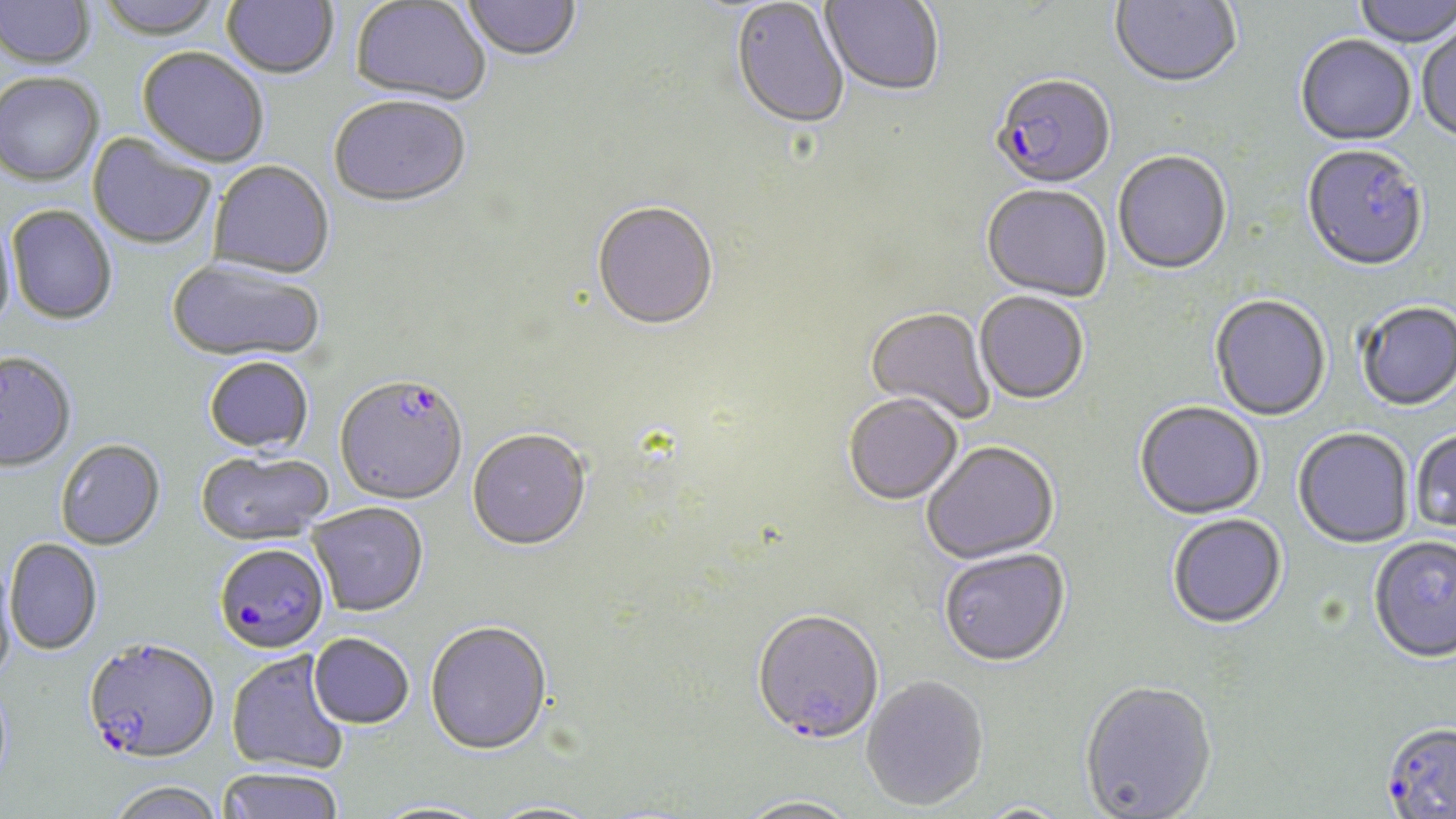 Approximate bounding boxes as (x1,y1)-(x2,y2) corner pairs in pixels. Uninfected red blood cell locations: (93,0)-(226,43), (221,0)-(340,82), (820,0)-(944,98), (1109,0)-(1242,90), (1353,0)-(1455,50), (0,1)-(96,73), (350,1)-(491,107), (461,1)-(583,64), (730,1)-(849,133), (1417,22)-(1456,145), (1295,37)-(1416,149), (137,49)-(269,170), (0,75)-(104,189), (329,99)-(472,212), (86,133)-(216,251), (1301,148)-(1428,275), (1113,152)-(1232,276), (207,163)-(335,281), (981,186)-(1111,304), (591,204)-(719,334), (6,206)-(117,327), (0,215)-(17,339), (166,260)-(325,365), (974,294)-(1088,406), (1209,296)-(1332,422), (1356,303)-(1456,413), (865,309)-(995,425), (0,354)-(77,475), (203,358)-(314,457), (844,396)-(963,508), (1134,403)-(1265,522), (1293,430)-(1414,550), (467,431)-(592,554), (1411,431)-(1456,534), (55,441)-(166,552), (922,443)-(1060,566), (195,453)-(334,547), (307,503)-(428,618), (1167,516)-(1287,631), (1368,538)-(1456,666), (4,539)-(102,655), (939,550)-(1071,670), (0,557)-(16,685), (752,613)-(885,748), (425,623)-(553,758), (309,635)-(414,731), (226,652)-(350,776), (861,677)-(989,813), (1079,682)-(1218,819), (215,769)-(345,819), (105,784)-(227,819), (733,798)-(863,819), (368,801)-(493,819). Plasmodium falciparum-infected red blood cell locations: (990,77)-(1116,192), (334,378)-(468,507), (214,545)-(329,654), (82,639)-(219,768), (1380,725)-(1456,818). Slide-level diagnosis: Plasmodium falciparum. One field of a larger specimen. Image is 1456×819 pixels. Captured at 1000x magnification. Thin blood smear. May-Grünwald-Giemsa-stained preparation. Optical microscopy.